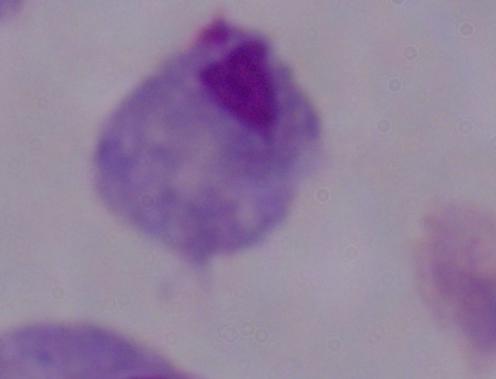
magnification = 1000x
modality = photomicrograph
identification = trichomonad